Classify this cell by malaria status.
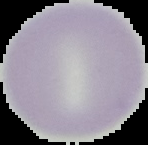
It is uninfected.

The area outside the segmented cell region is set to black. Image is 148×145 pixels. From a thin blood film.